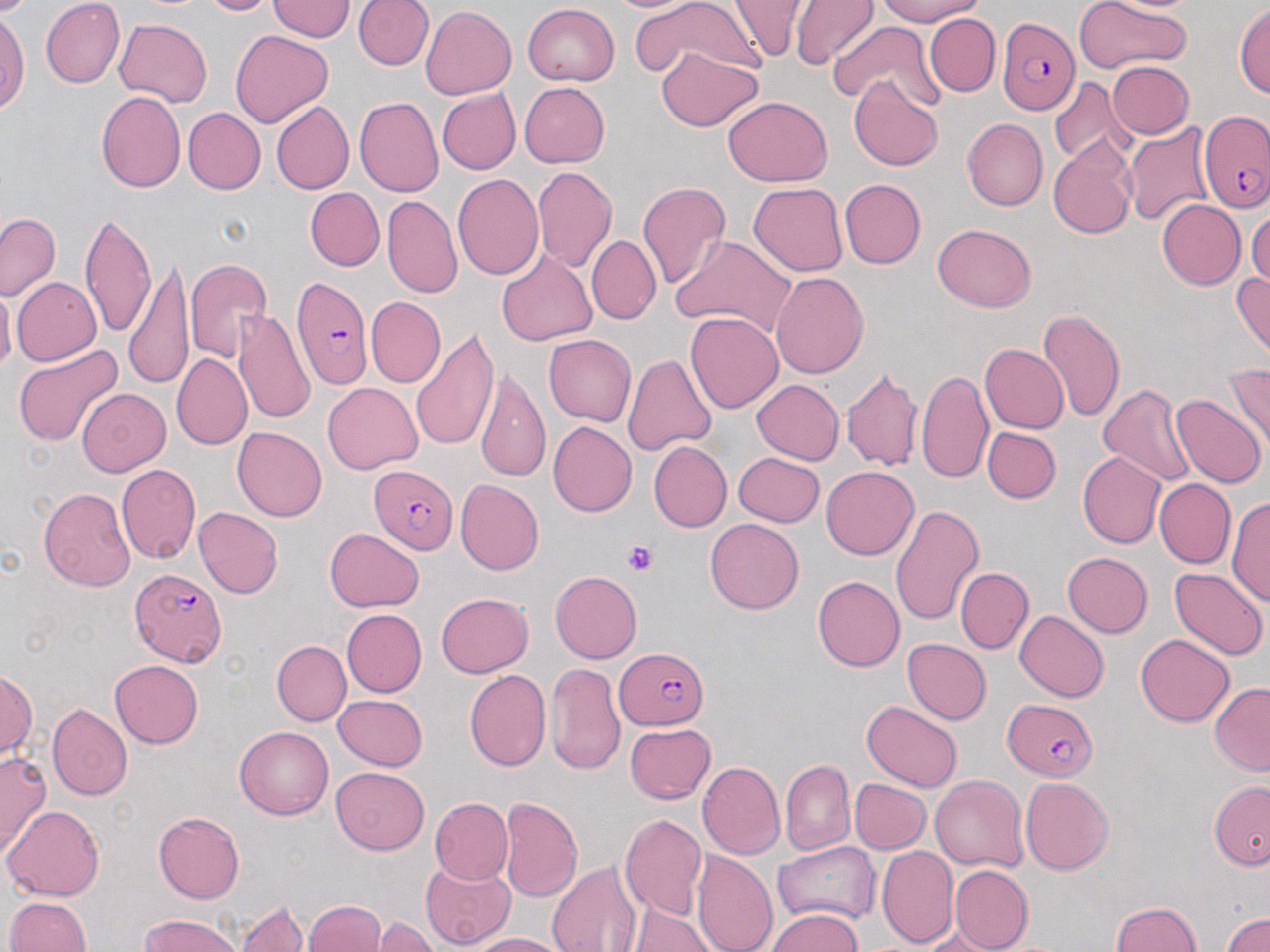
Approximate bounding boxes as (x1, y1, x2, y2) in pixels. Platelet locations: (622, 541, 658, 577). Uninfected red blood cell locations: (41, 0, 125, 89), (201, 0, 282, 16), (352, 0, 432, 71), (604, 0, 707, 14), (629, 0, 765, 81), (725, 0, 806, 62), (874, 0, 986, 25), (1074, 0, 1192, 73), (1091, 0, 1204, 14), (267, 1, 352, 40), (791, 1, 878, 69), (522, 3, 619, 86), (1233, 3, 1270, 98), (421, 6, 517, 99), (0, 9, 30, 113), (924, 14, 1000, 97), (115, 17, 212, 107), (829, 22, 937, 107), (230, 28, 333, 128), (655, 47, 762, 131), (1107, 61, 1194, 139), (849, 75, 943, 172), (1049, 77, 1131, 167), (519, 82, 610, 168), (437, 88, 520, 175), (96, 91, 186, 194), (355, 95, 445, 197), (723, 95, 831, 186), (271, 101, 354, 194), (183, 108, 266, 195), (961, 117, 1047, 211), (1122, 122, 1216, 228), (1048, 136, 1137, 240), (532, 166, 617, 274), (452, 174, 543, 281), (839, 179, 926, 269), (637, 181, 731, 290), (748, 181, 848, 277), (305, 187, 384, 271), (382, 195, 462, 299), (1156, 199, 1246, 290), (1247, 206, 1270, 290), (0, 212, 60, 302), (5, 212, 80, 372), (79, 213, 156, 339), (932, 222, 1036, 311), (673, 235, 799, 342), (587, 236, 661, 324), (495, 251, 599, 345), (123, 257, 194, 392), (183, 259, 273, 361), (1231, 270, 1270, 361), (771, 272, 869, 379), (13, 277, 102, 367), (0, 286, 15, 375), (366, 297, 446, 388), (1038, 308, 1126, 424), (234, 310, 315, 428), (686, 312, 783, 412), (410, 327, 500, 451), (544, 335, 636, 426), (11, 343, 124, 446), (979, 343, 1068, 434), (624, 352, 718, 456), (171, 353, 252, 450), (1224, 364, 1270, 460), (841, 367, 922, 472), (476, 369, 551, 483), (916, 370, 994, 484), (751, 379, 843, 465), (322, 382, 423, 473), (1098, 383, 1199, 487), (77, 389, 170, 476), (1169, 394, 1266, 487), (548, 421, 636, 517), (232, 426, 327, 521), (982, 427, 1061, 503), (648, 441, 732, 533), (1078, 451, 1165, 549), (733, 452, 824, 527), (116, 464, 202, 564), (822, 465, 918, 560), (1154, 478, 1235, 569), (455, 479, 544, 576), (38, 487, 136, 592), (1228, 495, 1269, 608), (891, 505, 983, 627), (193, 507, 283, 598), (705, 518, 804, 614), (324, 528, 424, 611), (1062, 553, 1153, 638), (955, 566, 1034, 653), (1168, 567, 1268, 661), (550, 570, 643, 664), (813, 576, 905, 672), (435, 593, 534, 678), (341, 609, 427, 697), (1015, 610, 1109, 703), (1135, 633, 1234, 726), (902, 638, 992, 725), (271, 640, 352, 727), (109, 659, 203, 749), (546, 662, 626, 776), (0, 669, 36, 762), (464, 669, 551, 771), (1210, 682, 1270, 774), (333, 694, 428, 771), (861, 700, 963, 793), (48, 703, 132, 801), (624, 723, 714, 804), (234, 726, 333, 819), (1, 752, 51, 858), (781, 758, 855, 855), (697, 762, 784, 859), (331, 767, 428, 854), (930, 774, 1028, 871), (1020, 777, 1113, 874), (850, 778, 931, 854), (1209, 781, 1270, 868), (499, 795, 583, 903), (429, 797, 513, 884), (3, 804, 106, 901), (153, 810, 244, 904), (619, 812, 707, 922), (773, 842, 879, 926), (876, 845, 958, 947), (691, 849, 777, 952), (419, 858, 515, 949), (547, 860, 642, 952), (949, 865, 1033, 952), (4, 896, 91, 952), (235, 899, 309, 952), (302, 900, 386, 952), (1109, 902, 1201, 952), (627, 904, 718, 952), (768, 908, 863, 951), (1222, 911, 1270, 952), (138, 913, 245, 952), (367, 917, 440, 951), (919, 928, 1006, 951), (464, 932, 567, 952). Plasmodium falciparum-infected red blood cell locations: (997, 18, 1077, 115), (1200, 110, 1267, 213), (290, 277, 374, 391), (369, 466, 459, 554), (129, 568, 226, 667), (615, 647, 709, 729), (1003, 698, 1098, 781). Slide-level diagnosis: Plasmodium falciparum. Image is 1270×952 pixels. Optical microscopy. May-Grünwald-Giemsa-stained preparation. Thin blood smear. Single field of view. Captured at 1000x magnification.